Comment on the morphology of the erythrocytes.
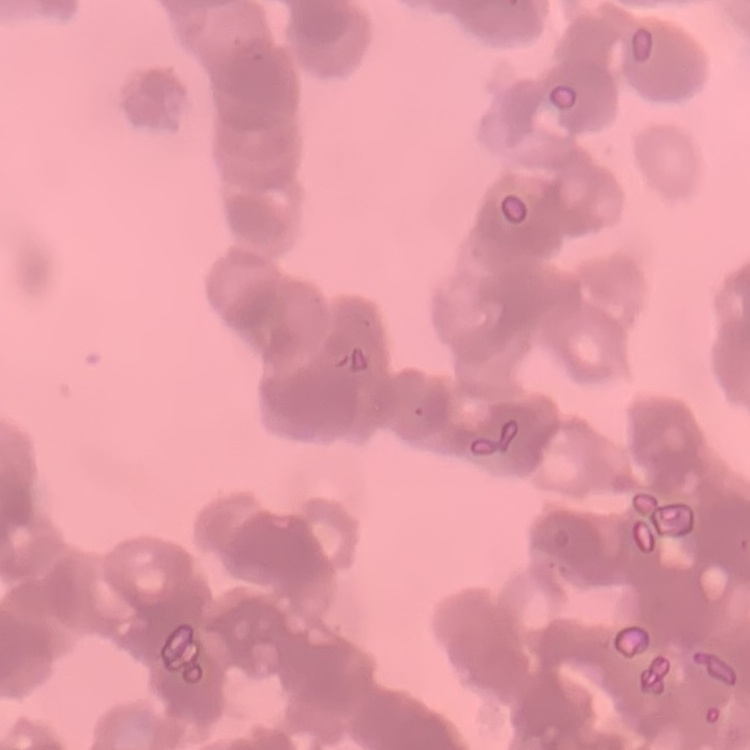

They show rouleaux formation.

preparation: thin peripheral smear
stain: Field's or Giemsa
image_type: square crop of a larger photomicrograph